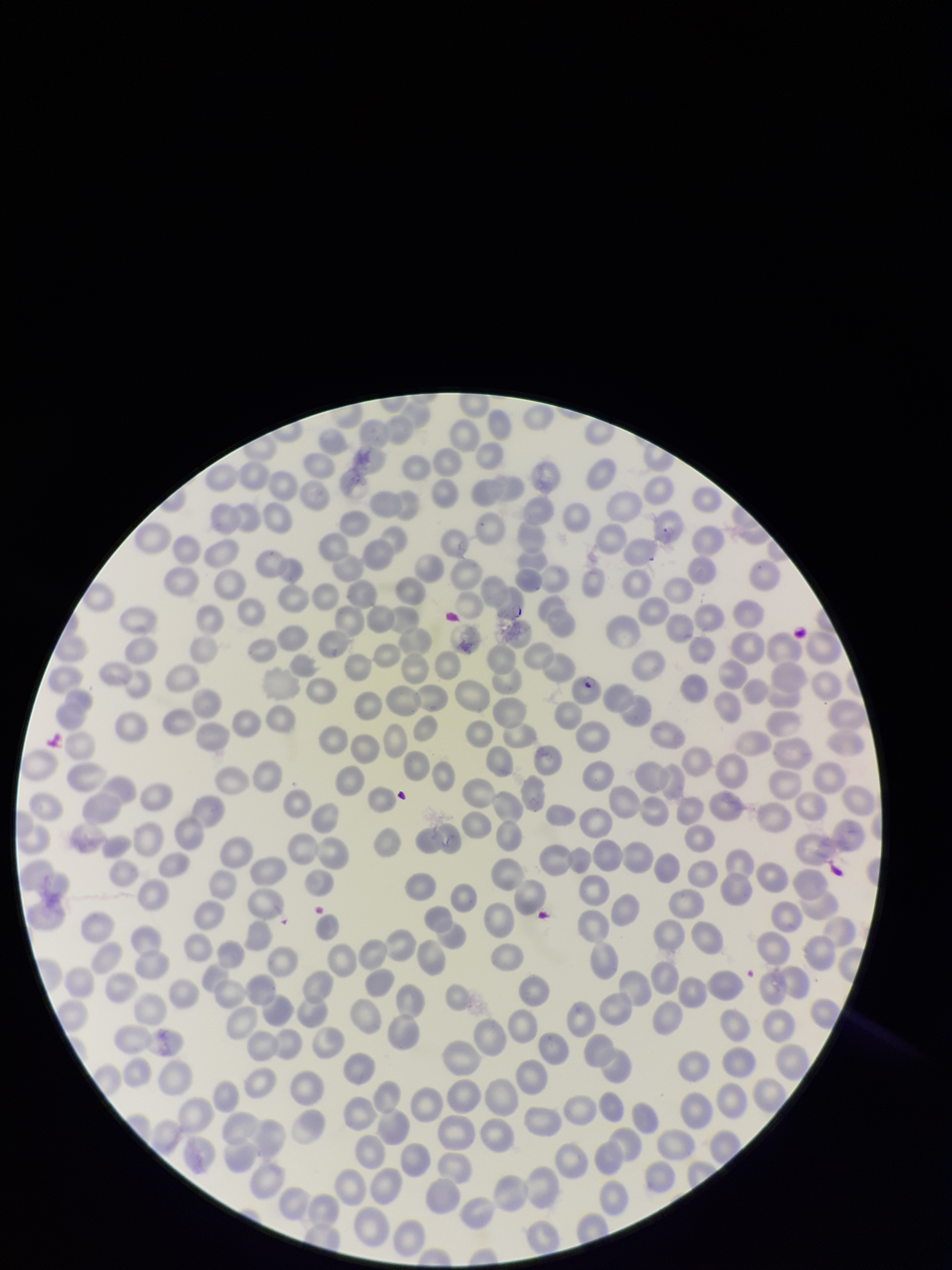

Summary:
  - Preparation: thin smear
  - Field of view: one from this slide
  - Parasitized red blood cell count: 1
  - Patient malaria status: infected
  - Capture: smartphone photograph through the microscope eyepiece
  - Red blood cell count: 324
  - Stain: Giemsa
  - Parasitized red blood cells: detected
  - Species reported for this patient: Plasmodium falciparum
  - Image size: 952×1270 pixels